Report the malaria status of this cell.
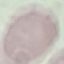
Uninfected.

Summary:
  - Preparation: thin blood film
  - Stain: Giemsa
  - Image type: cell patch, automatically extracted from a larger field of view and resized to 64 × 64 pixels
  - Capture: smartphone camera at the microscope eyepiece